Point out each Plasmodium parasite.
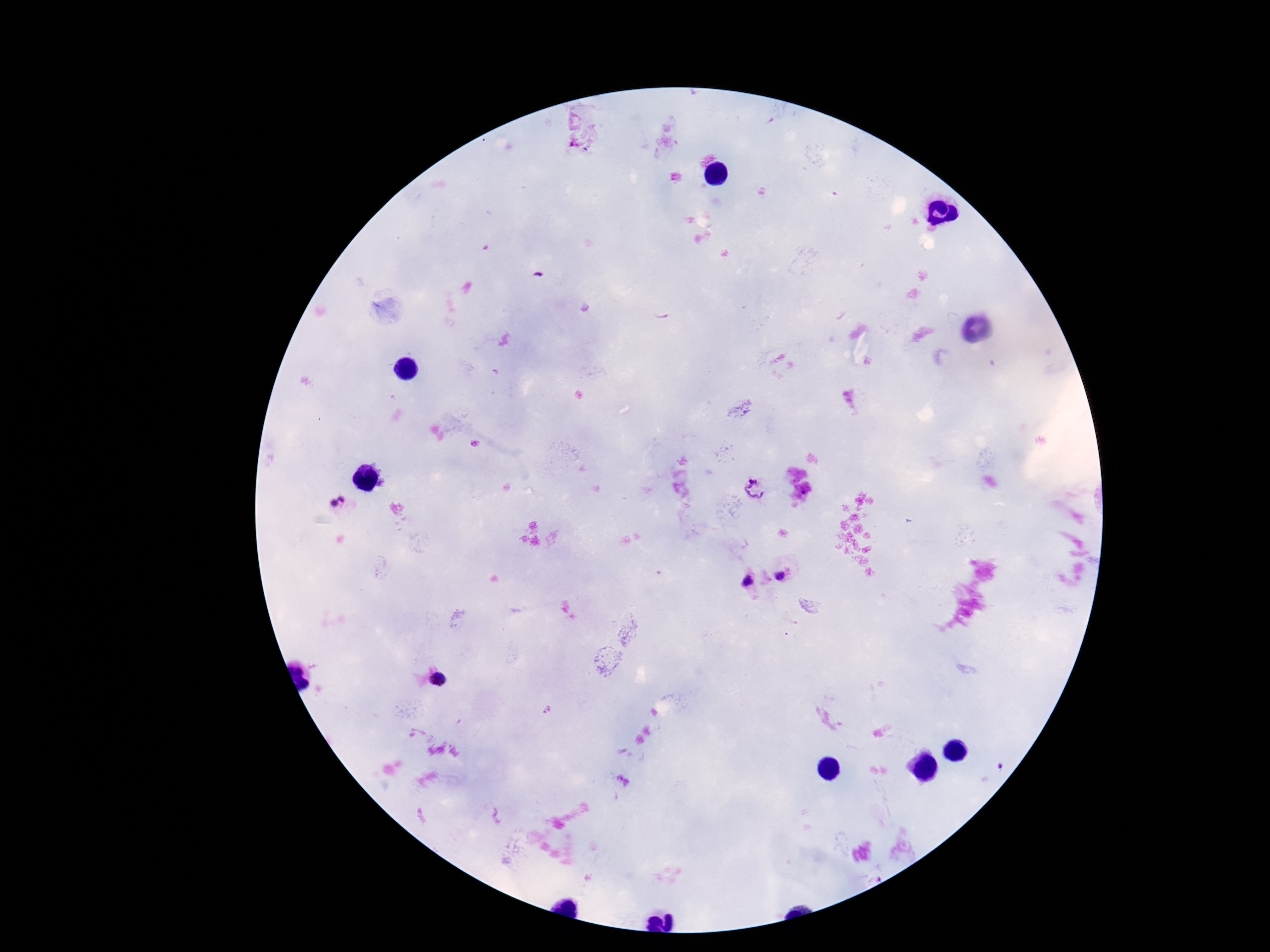

Approximate centers as (x, y) in pixels.
Plasmodium parasites: (759, 489), (336, 503), (784, 576), (751, 584), (438, 680).

Image is 1270×952 pixels. 100x magnification. Giemsa stain. Patient malaria status: positive. Single field of view. Photographed through the microscope eyepiece with a smartphone camera. Thick blood film.